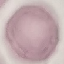
Summary:
  - Result: negative for malaria parasites
  - Stain: Giemsa
  - Preparation: thin blood film
  - Capture: smartphone through the microscope eyepiece
  - Image type: cell patch, automatically extracted from a larger field of view and resized to 64 × 64 pixels